Classify this cell by malaria status.
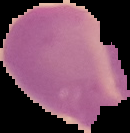
Uninfected.

Summary:
  - Image size: 130×133 pixels
  - Preparation: thin blood film
  - Image type: cell region segmented out of the field of view; surrounding area masked to black